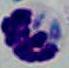
Photomicrograph. A leukocyte is shown. Captured at 1000x magnification.